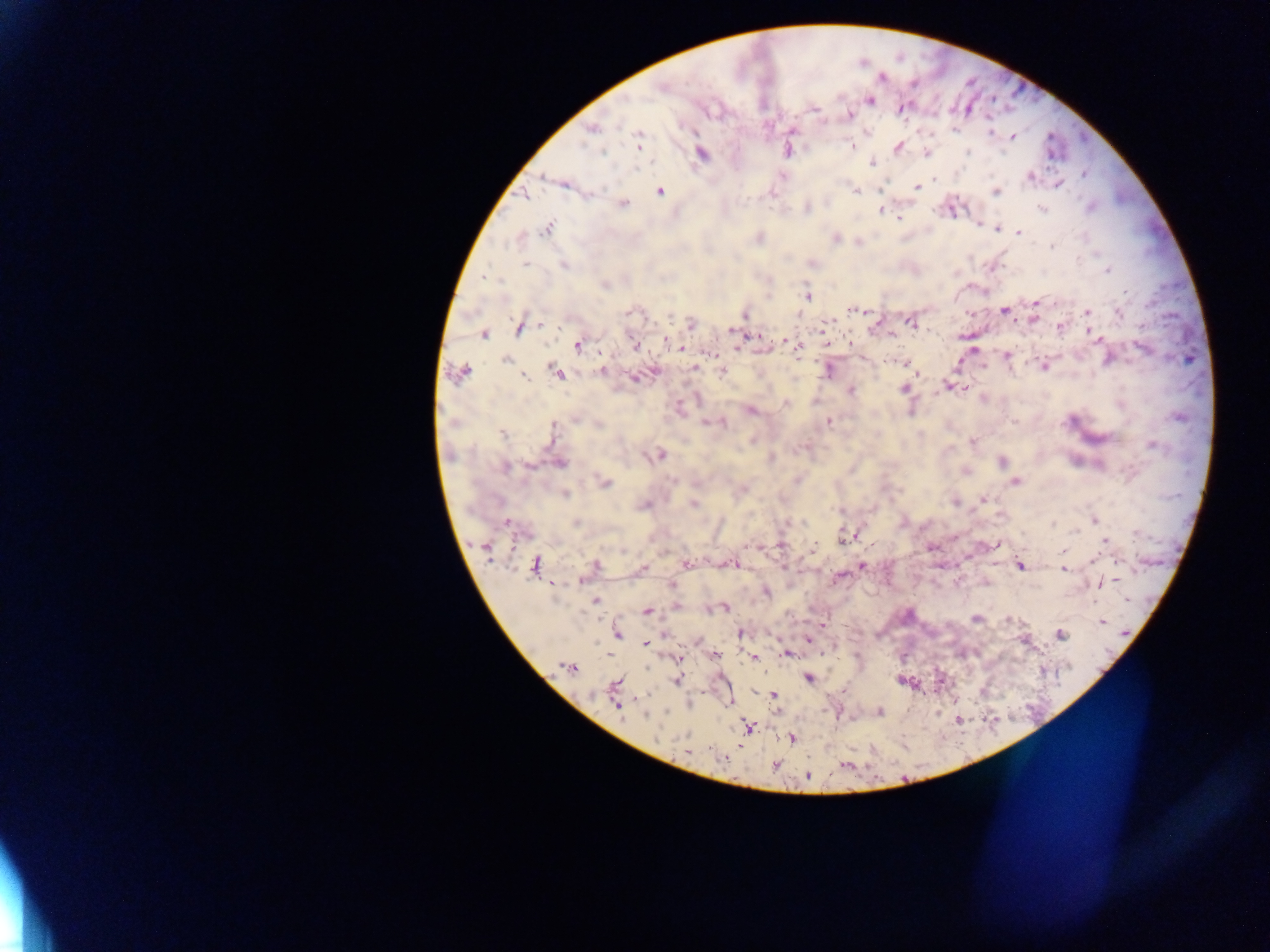

Approximate centers as x y in pixels. Plasmodium parasite locations: 661 87; 870 100; 901 108; 849 116; 591 129; 955 129; 990 132; 1013 136; 639 138; 852 146; 898 147; 788 151; 968 151; 602 152; 926 152; 701 153; 872 163; 638 168; 1084 174; 543 176; 782 177; 1030 177; 934 179; 1059 185; 917 188; 880 190; 857 191; 661 192; 995 192; 525 195; 624 204; 1090 207; 807 208; 1042 208; 881 210; 899 218; 978 226; 547 228; 996 228; 1002 229; 1018 232; 759 238; 836 239; 1052 246; 812 263; 526 264; 564 266; 1107 271; 486 277; 604 285; 1126 292; 808 297; 1035 303; 854 310; 1004 310; 1087 312; 630 313; 1119 314; 744 315; 670 317; 1034 319; 912 323; 690 324; 540 325; 1060 327; 519 328; 731 331; 483 334; 893 335; 754 336; 1097 338; 666 341; 787 341; 578 346; 634 346; 677 346; 738 347; 1142 348; 797 350; 973 350; 709 353; 1006 355; 506 360; 905 364; 1044 366; 694 367; 828 370; 600 371; 461 372; 556 372; 722 372; 525 378; 634 378; 946 385; 964 388; 904 389; 851 391; 786 403; 679 407; 751 411; 575 419; 829 421; 707 423; 722 423; 600 425; 553 432; 503 435; 972 442; 1152 445; 660 454; 1002 461; 560 463; 530 466; 504 468; 1016 481; 605 482; 744 489; 566 495; 984 499; 955 503; 694 505; 643 506; 1094 520; 575 523; 1053 523; 508 524; 1078 530; 847 536; 1106 541; 996 544; 747 547; 813 548; 486 549; 1062 551; 1093 559; 687 564; 731 565; 1021 565; 534 566; 594 566; 861 566; 643 568; 1064 570; 581 580; 1113 580; 1102 581; 672 585; 767 592; 595 601; 677 606; 724 608; 647 611; 976 618; 1009 620; 1102 621; 823 624; 741 633; 618 634; 1060 635; 807 639; 645 644; 786 654; 716 655; 754 657; 679 659; 569 667; 808 678; 677 680; 616 684; 774 695; 617 705; 879 712; 645 716; 959 720; 748 727; 792 739; 686 751; 724 759; 775 765; 807 777. Mobile-phone photograph taken through the microscope. Thick blood film. Single field of view. Sample from Ghana. Image is 1270×952 pixels.